Assess the morphology of the erythrocytes.
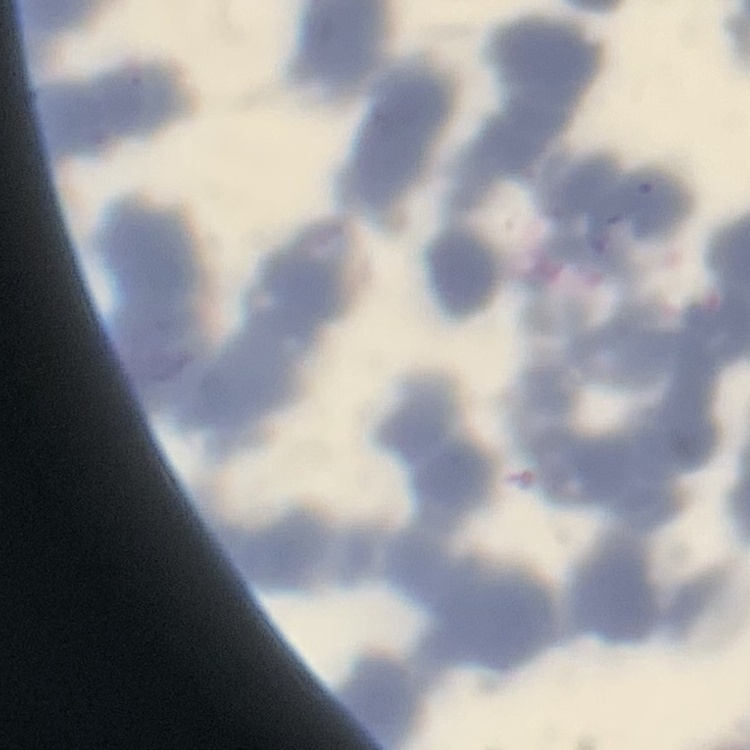

Rouleaux formation.

Thin blood film. Stained with either Field's or Giemsa. One tile cut from a larger photomicrograph.